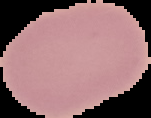
From a thin blood smear. Image is 151×118 pixels. Malaria status: uninfected. Segmented cell region on a black background.